State which parasite is depicted.
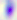

Toxoplasma gondii.

Summary:
  - Modality: photomicrograph
  - Magnification: 400x